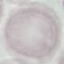
{
  "malaria_status": "uninfected",
  "preparation": "thin blood smear",
  "capture": "smartphone through the microscope eyepiece",
  "stain": "Giemsa",
  "image_type": "automatically extracted cell patch, resized to 64 × 64 pixels"
}